Locate every blood parasite and identify its species.
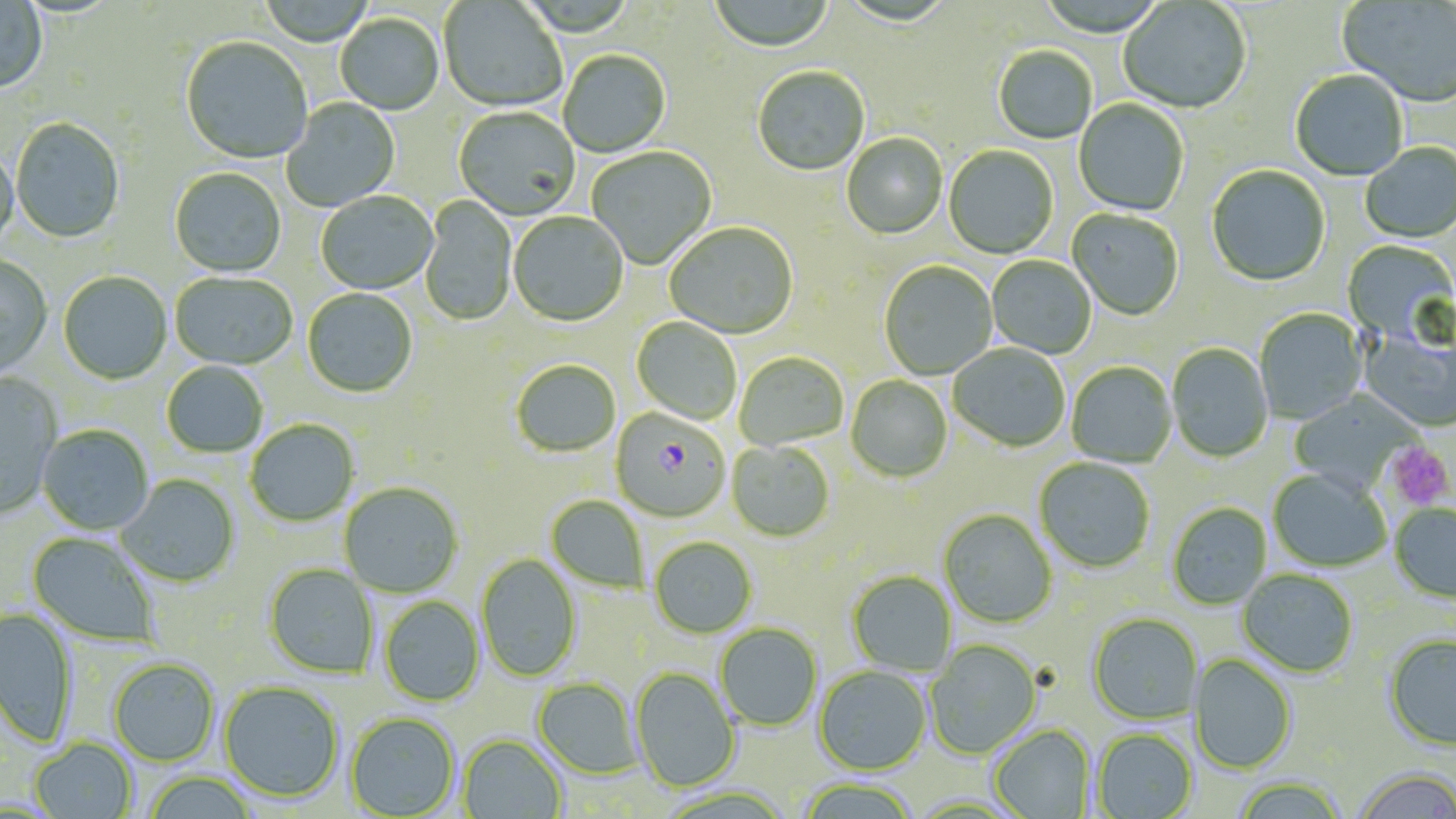

Approximate bounding boxes as named x1/y1/x2/y2 corners in pixels.
Plasmodium falciparum-infected red blood cells: (x1=609, y1=410, x2=730, y2=524).
No Plasmodium ovale, Plasmodium malariae, Plasmodium vivax, Babesia divergens, or Trypanosoma brucei observed.

Uninfected red blood cell locations: (x1=708, y1=0, x2=834, y2=54), (x1=0, y1=1, x2=48, y2=94), (x1=439, y1=1, x2=566, y2=113), (x1=1118, y1=1, x2=1251, y2=115), (x1=1338, y1=1, x2=1456, y2=108), (x1=335, y1=15, x2=444, y2=116), (x1=180, y1=38, x2=312, y2=166), (x1=993, y1=47, x2=1097, y2=145), (x1=559, y1=51, x2=671, y2=159), (x1=752, y1=67, x2=870, y2=178), (x1=1290, y1=71, x2=1408, y2=182), (x1=281, y1=98, x2=400, y2=211), (x1=1073, y1=99, x2=1189, y2=218), (x1=454, y1=108, x2=580, y2=221), (x1=10, y1=119, x2=125, y2=244), (x1=842, y1=134, x2=948, y2=240), (x1=1361, y1=144, x2=1456, y2=244), (x1=0, y1=146, x2=19, y2=254), (x1=943, y1=146, x2=1058, y2=260), (x1=586, y1=147, x2=717, y2=271), (x1=1206, y1=166, x2=1330, y2=288), (x1=169, y1=168, x2=286, y2=278), (x1=316, y1=192, x2=438, y2=296), (x1=419, y1=196, x2=517, y2=328), (x1=1067, y1=209, x2=1183, y2=321), (x1=508, y1=212, x2=629, y2=328), (x1=664, y1=223, x2=798, y2=340), (x1=1341, y1=240, x2=1456, y2=348), (x1=0, y1=255, x2=52, y2=378), (x1=986, y1=256, x2=1096, y2=359), (x1=879, y1=262, x2=997, y2=380), (x1=58, y1=273, x2=172, y2=385), (x1=170, y1=273, x2=297, y2=371), (x1=302, y1=289, x2=418, y2=399), (x1=1254, y1=309, x2=1367, y2=426), (x1=632, y1=318, x2=742, y2=425), (x1=1359, y1=328, x2=1456, y2=434), (x1=1166, y1=344, x2=1273, y2=464), (x1=948, y1=345, x2=1070, y2=453), (x1=734, y1=353, x2=848, y2=451), (x1=511, y1=361, x2=621, y2=457), (x1=161, y1=362, x2=268, y2=458), (x1=1066, y1=363, x2=1176, y2=468), (x1=0, y1=372, x2=62, y2=520), (x1=846, y1=375, x2=953, y2=483), (x1=1288, y1=391, x2=1416, y2=493), (x1=245, y1=420, x2=359, y2=527), (x1=37, y1=425, x2=154, y2=535), (x1=726, y1=442, x2=834, y2=543), (x1=1034, y1=458, x2=1155, y2=574), (x1=1268, y1=470, x2=1390, y2=572), (x1=116, y1=475, x2=240, y2=588), (x1=339, y1=482, x2=463, y2=598), (x1=545, y1=496, x2=648, y2=593), (x1=1167, y1=503, x2=1272, y2=610), (x1=1389, y1=504, x2=1456, y2=605), (x1=938, y1=510, x2=1056, y2=629), (x1=27, y1=532, x2=161, y2=646), (x1=649, y1=537, x2=757, y2=639), (x1=476, y1=554, x2=582, y2=682), (x1=263, y1=564, x2=378, y2=679), (x1=1237, y1=570, x2=1358, y2=679), (x1=846, y1=571, x2=956, y2=676), (x1=380, y1=596, x2=484, y2=706), (x1=0, y1=607, x2=78, y2=747), (x1=1088, y1=614, x2=1203, y2=725), (x1=715, y1=623, x2=823, y2=731), (x1=1383, y1=635, x2=1456, y2=753), (x1=925, y1=640, x2=1042, y2=759), (x1=1189, y1=654, x2=1297, y2=775), (x1=108, y1=658, x2=219, y2=766), (x1=814, y1=665, x2=931, y2=775), (x1=631, y1=668, x2=740, y2=793), (x1=533, y1=677, x2=644, y2=779), (x1=218, y1=680, x2=344, y2=803), (x1=345, y1=712, x2=460, y2=817), (x1=989, y1=724, x2=1095, y2=819), (x1=1092, y1=729, x2=1198, y2=819), (x1=458, y1=734, x2=567, y2=819), (x1=29, y1=737, x2=138, y2=819), (x1=1350, y1=770, x2=1456, y2=819), (x1=142, y1=772, x2=259, y2=819), (x1=1232, y1=778, x2=1349, y2=819), (x1=794, y1=779, x2=921, y2=819). Platelet locations: (x1=1386, y1=442, x2=1453, y2=510). Slide-level diagnosis: Plasmodium falciparum. May-Grünwald-Giemsa-stained preparation. Image is 1456×819 pixels. Light microscopy. Thin blood film. 1000x magnification. One field of a larger specimen.